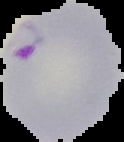
Cell region segmented out of the field of view; the surrounding area is masked to black. Image is 124×142 pixels. From a thin blood film. Result: Plasmodium parasites detected.